Assess this cell for malaria.
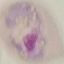

Parasitized.

Photographed with a smartphone camera at the microscope eyepiece. Giemsa-stained preparation. Thin blood smear. Automatically extracted cell patch, resized to 64 × 64 pixels.